Give the position of every malaria parasite.
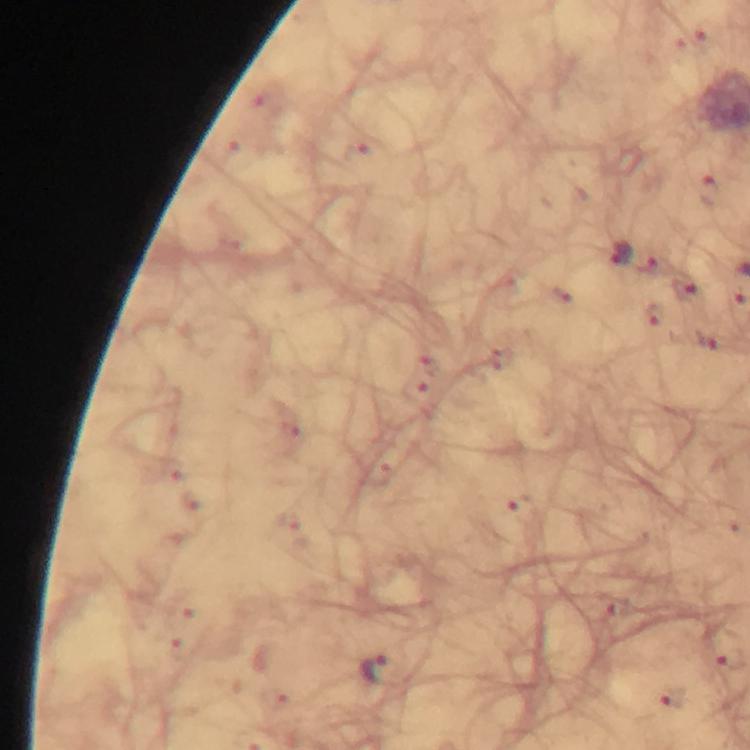

Approximate centers as (x, y) in pixels.
Malaria parasites: (619, 255), (375, 672).

Immersion oil applied. Cropped region of a single field of view. Thick blood film. Giemsa-stained preparation. Photographed through the microscope with a smartphone camera. At 100x magnification. Image is 750×750 pixels. From a malaria diagnostic workup.